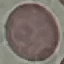 Malaria status: uninfected. Acquired by smartphone through the microscope eyepiece. Giemsa stain. Thin blood smear. Automatically extracted cell patch, resized to 64 × 64 pixels.